State the blood parasite species.
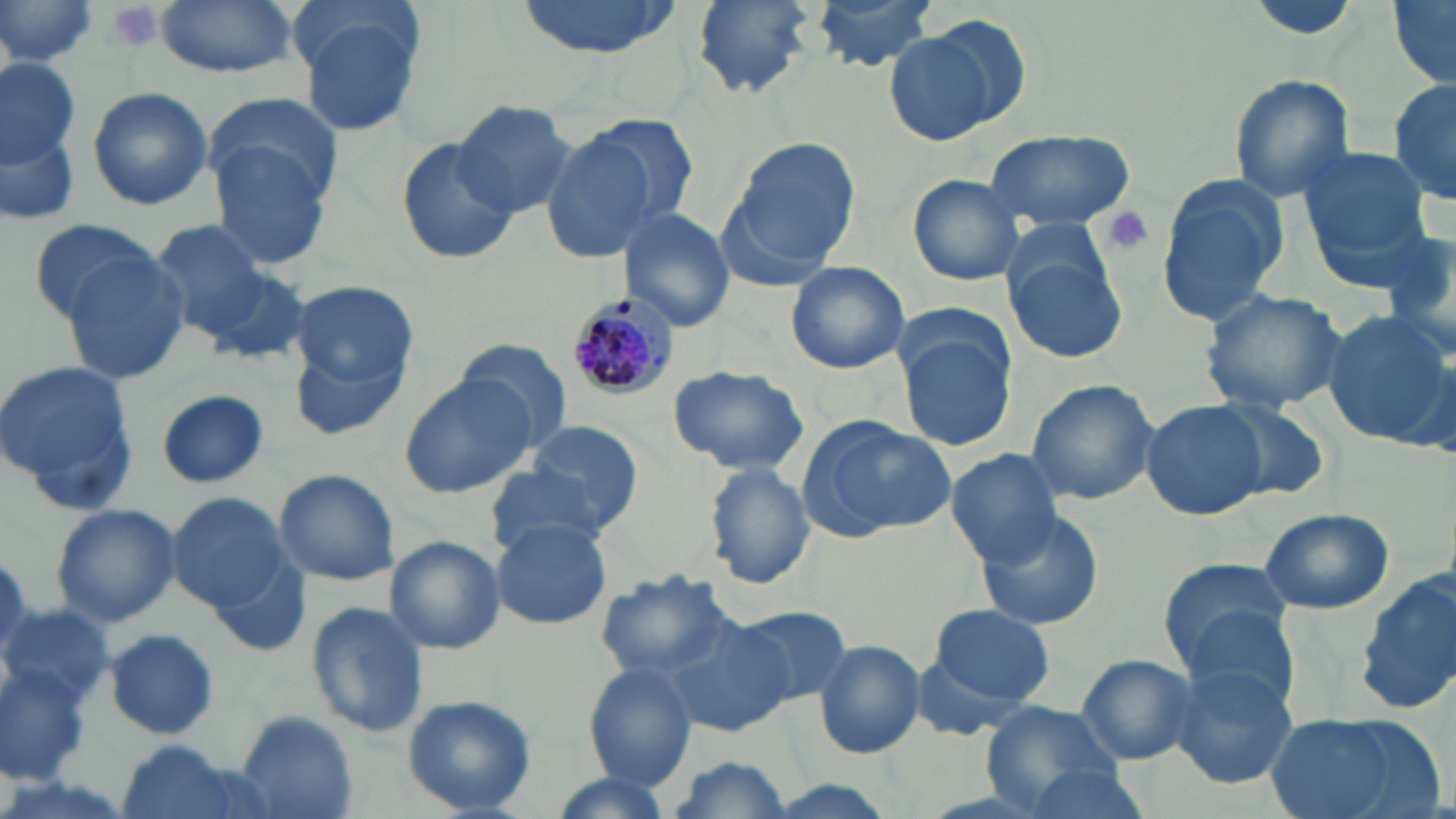
Plasmodium malariae.

{
  "preparation": "thin blood film",
  "plasmodium_malariae_infected_red_blood_cell_locations": "approximate bounding boxes as named x1/y1/x2/y2 corners in pixels: (x1=573, y1=297, x2=679, y2=400)",
  "field_of_view": "single",
  "modality": "optical microscopy",
  "platelet_locations": "approximate bounding boxes as named x1/y1/x2/y2 corners in pixels: (x1=103, y1=3, x2=163, y2=52), (x1=1102, y1=207, x2=1157, y2=257)",
  "magnification": "1000x",
  "stain": "May-Grünwald-Giemsa",
  "uninfected_red_blood_cell_locations": "approximate bounding boxes as named x1/y1/x2/y2 corners in pixels: (x1=0, y1=0, x2=99, y2=75), (x1=153, y1=0, x2=299, y2=77), (x1=512, y1=0, x2=683, y2=57), (x1=691, y1=0, x2=818, y2=100), (x1=810, y1=0, x2=940, y2=73), (x1=1387, y1=0, x2=1455, y2=87), (x1=296, y1=9, x2=429, y2=138), (x1=882, y1=17, x2=1026, y2=145), (x1=0, y1=58, x2=81, y2=166), (x1=1226, y1=74, x2=1357, y2=204), (x1=1390, y1=76, x2=1456, y2=207), (x1=86, y1=87, x2=213, y2=211), (x1=204, y1=91, x2=346, y2=211), (x1=449, y1=98, x2=580, y2=217), (x1=575, y1=110, x2=702, y2=232), (x1=0, y1=121, x2=80, y2=229), (x1=537, y1=129, x2=661, y2=264), (x1=983, y1=129, x2=1135, y2=233), (x1=206, y1=135, x2=336, y2=271), (x1=724, y1=136, x2=863, y2=280), (x1=396, y1=139, x2=518, y2=266), (x1=1299, y1=147, x2=1435, y2=267), (x1=907, y1=173, x2=1028, y2=286), (x1=1157, y1=173, x2=1290, y2=327), (x1=618, y1=209, x2=736, y2=330), (x1=26, y1=218, x2=168, y2=325), (x1=149, y1=220, x2=270, y2=337), (x1=1373, y1=230, x2=1456, y2=341), (x1=1003, y1=241, x2=1131, y2=366), (x1=59, y1=246, x2=193, y2=383), (x1=199, y1=259, x2=313, y2=365), (x1=783, y1=261, x2=911, y2=375), (x1=292, y1=281, x2=419, y2=392), (x1=1199, y1=288, x2=1351, y2=415), (x1=1319, y1=308, x2=1456, y2=449), (x1=288, y1=321, x2=413, y2=446), (x1=895, y1=322, x2=1019, y2=453), (x1=455, y1=338, x2=574, y2=450), (x1=0, y1=357, x2=141, y2=512), (x1=665, y1=365, x2=809, y2=477), (x1=398, y1=371, x2=540, y2=499), (x1=1023, y1=379, x2=1160, y2=506), (x1=156, y1=388, x2=271, y2=488), (x1=1140, y1=399, x2=1272, y2=522), (x1=1207, y1=399, x2=1330, y2=502), (x1=798, y1=416, x2=957, y2=541), (x1=521, y1=420, x2=647, y2=533), (x1=946, y1=448, x2=1065, y2=566), (x1=703, y1=462, x2=814, y2=591), (x1=483, y1=463, x2=614, y2=558), (x1=272, y1=468, x2=400, y2=585), (x1=166, y1=490, x2=290, y2=611), (x1=50, y1=502, x2=183, y2=627), (x1=974, y1=506, x2=1104, y2=631), (x1=1257, y1=507, x2=1394, y2=614), (x1=489, y1=518, x2=613, y2=631), (x1=385, y1=535, x2=506, y2=655), (x1=202, y1=550, x2=314, y2=657), (x1=1159, y1=560, x2=1300, y2=673), (x1=1356, y1=567, x2=1456, y2=716), (x1=593, y1=572, x2=736, y2=682), (x1=305, y1=599, x2=427, y2=740), (x1=0, y1=600, x2=118, y2=716), (x1=927, y1=604, x2=1056, y2=709), (x1=727, y1=605, x2=851, y2=711), (x1=1180, y1=606, x2=1301, y2=713), (x1=662, y1=615, x2=794, y2=738), (x1=103, y1=628, x2=221, y2=741), (x1=813, y1=639, x2=926, y2=760), (x1=1074, y1=653, x2=1200, y2=765), (x1=1167, y1=662, x2=1297, y2=789), (x1=2, y1=663, x2=90, y2=784), (x1=584, y1=663, x2=698, y2=789), (x1=401, y1=694, x2=537, y2=816), (x1=977, y1=699, x2=1130, y2=812), (x1=234, y1=710, x2=359, y2=819), (x1=1259, y1=711, x2=1439, y2=819), (x1=112, y1=738, x2=257, y2=819), (x1=663, y1=756, x2=796, y2=819), (x1=1019, y1=763, x2=1154, y2=818), (x1=546, y1=773, x2=678, y2=819)",
  "image_size": "1456×819 pixels"
}